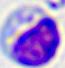

Summary:
  - Modality: micrograph
  - Identification: white blood cell
  - Magnification: 400x